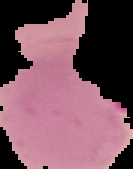

image_size: 133×169 pixels
preparation: thin blood smear
image_type: segmented cell region with the area outside set to black
malaria_status: parasitized